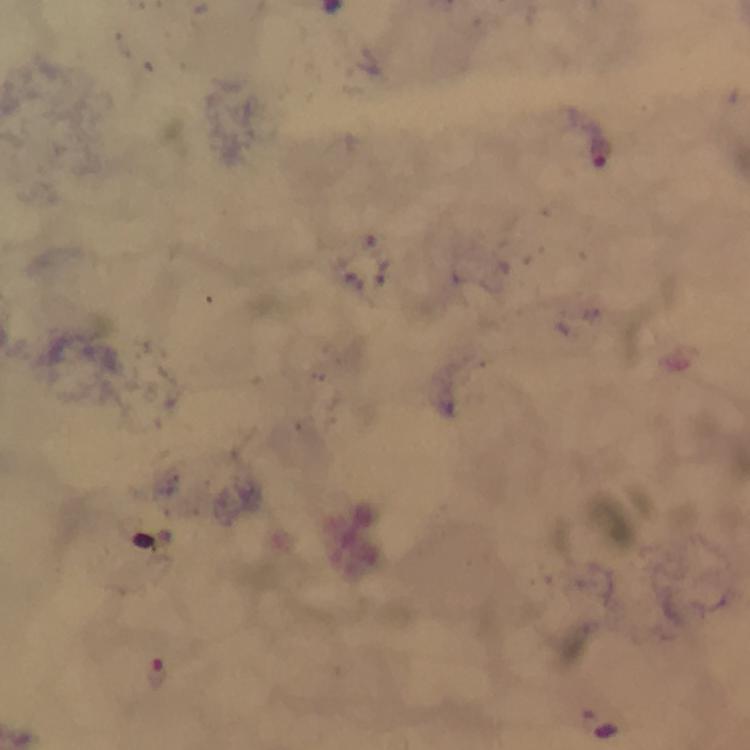

{
  "stain": "Giemsa",
  "image_size": "750×750 pixels",
  "context": "from a malaria diagnostic workup",
  "cropped_from": "one field of view",
  "immersion_oil": "used",
  "magnification": "100x",
  "preparation": "thick blood film",
  "capture": "smartphone photograph through a microscope",
  "malaria_parasite_locations": "approximate centers as {x, y} in pixels: {603, 151}, {156, 673}"
}